Assess this cell for malaria.
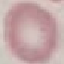

It is uninfected.

Summary:
  - Capture: smartphone camera at the microscope eyepiece
  - Preparation: thin smear
  - Image type: cell patch, automatically extracted from a larger field of view and resized to 64 × 64 pixels
  - Stain: Giemsa